Assess this cell for malaria.
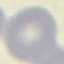
Uninfected.

Cell patch, automatically extracted from a larger field of view and resized to 64 × 64 pixels. Thin smear of blood. Giemsa stain. Photographed with a smartphone camera at the microscope eyepiece.